Outline each blood parasite and name the species.
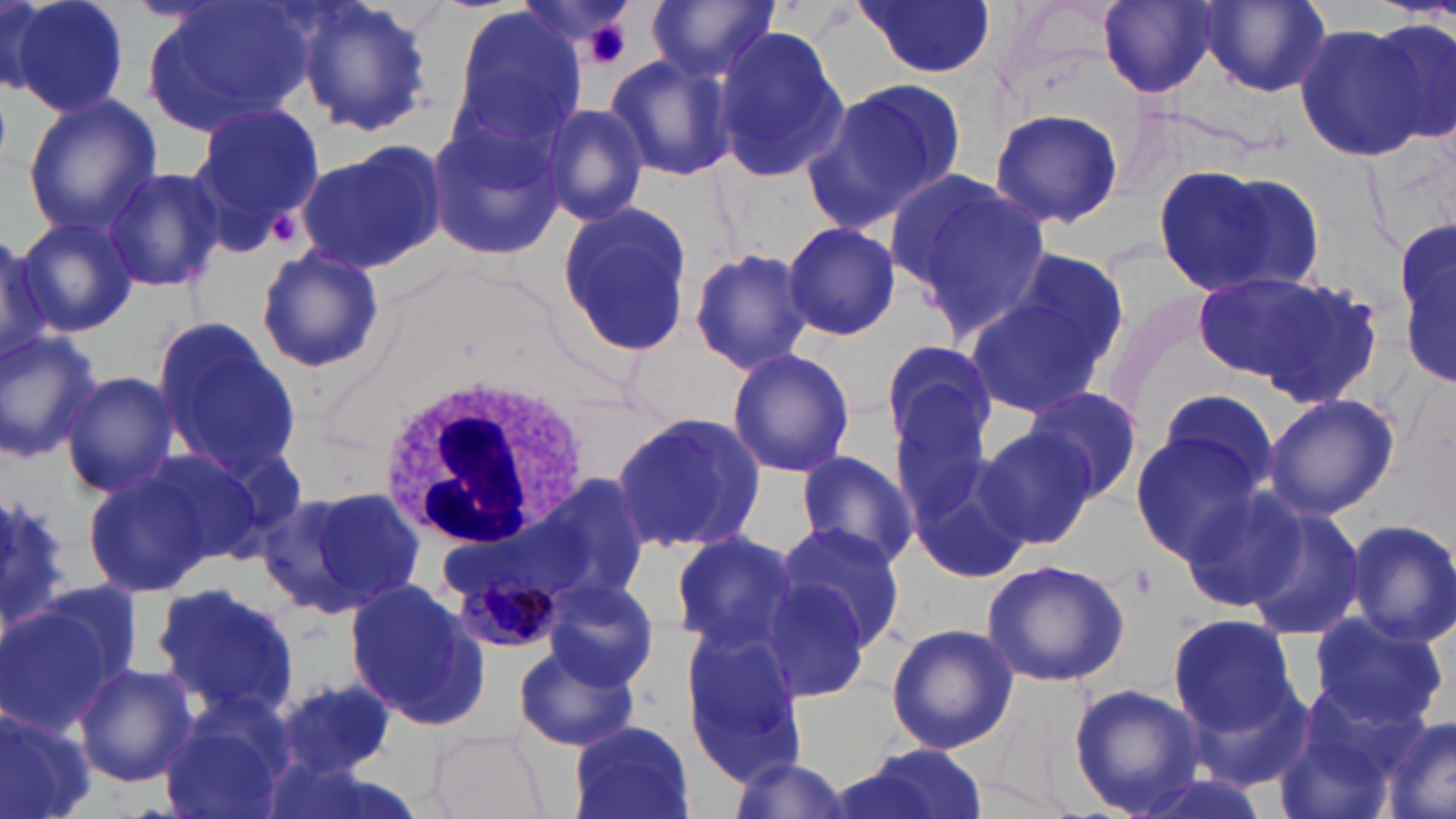

Approximate bounding boxes as (x1,y1)-(x2,y2) corner pairs in pixels.
Plasmodium malariae-infected red blood cells: (459,570)-(561,653).
No Plasmodium falciparum, Plasmodium ovale, Plasmodium vivax, Babesia divergens, or Trypanosoma brucei observed.

White blood cell locations: (375,371)-(591,552). Uninfected red blood cell locations: (6,0)-(130,119), (138,0)-(309,141), (292,0)-(433,139), (856,0)-(997,79), (1099,0)-(1219,99), (646,2)-(778,85), (1198,2)-(1331,97), (446,4)-(587,155), (1367,17)-(1454,143), (1292,21)-(1433,161), (712,27)-(848,185), (605,53)-(740,182), (811,75)-(966,230), (22,95)-(159,239), (187,102)-(325,246), (542,104)-(649,226), (989,106)-(1124,229), (429,113)-(566,261), (295,139)-(446,276), (1156,162)-(1324,301), (102,165)-(225,293), (887,169)-(1053,337), (555,202)-(694,359), (18,212)-(140,335), (1398,220)-(1454,394), (782,222)-(901,341), (0,228)-(53,366), (255,246)-(384,377), (994,246)-(1133,383), (687,248)-(813,374), (1190,268)-(1372,401), (963,284)-(1116,424), (151,316)-(301,480), (0,328)-(104,464), (877,340)-(997,468), (726,347)-(856,480), (61,372)-(181,499), (886,374)-(1011,540), (1150,385)-(1282,504), (1024,386)-(1142,502), (1263,392)-(1399,521), (610,410)-(767,556), (1130,424)-(1269,560), (977,426)-(1101,551), (905,438)-(1033,587), (794,449)-(919,569), (80,463)-(221,595), (526,473)-(654,611), (1177,485)-(1311,610), (274,486)-(425,616), (0,494)-(72,633), (1238,504)-(1368,644), (1344,517)-(1456,647), (774,521)-(908,652), (669,531)-(804,659), (980,558)-(1133,687), (754,575)-(873,702), (542,579)-(660,691), (151,581)-(300,718), (346,581)-(488,729), (4,592)-(132,734), (1308,610)-(1451,732), (1163,612)-(1303,742), (885,622)-(1019,755), (681,628)-(807,782), (514,639)-(640,752), (72,662)-(197,787), (274,676)-(396,779), (1067,683)-(1209,816), (0,704)-(97,819), (1272,704)-(1408,819), (160,708)-(289,819), (1379,715)-(1456,819), (567,720)-(694,819), (426,728)-(550,819), (841,746)-(986,819), (725,754)-(849,819). Platelet locations: (581,18)-(631,69), (1126,563)-(1157,599). Slide-level diagnosis: Plasmodium malariae. Image is 1456×819 pixels. Thin blood film. Optical microscopy. Captured at 1000x magnification. One field of a larger specimen. May-Grünwald-Giemsa stain.